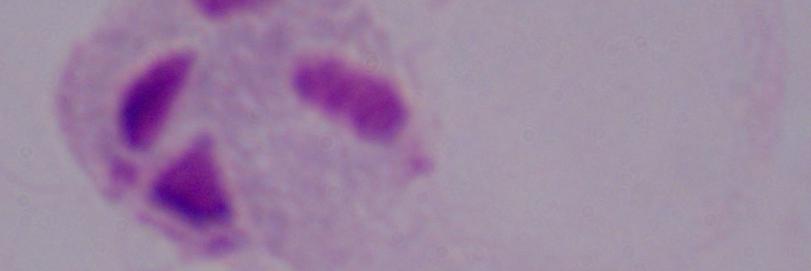

identification: trichomonad
magnification: 1000x
modality: micrograph